State which parasite is depicted.
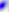
This is Toxoplasma gondii.

Photomicrograph. 400x magnification.